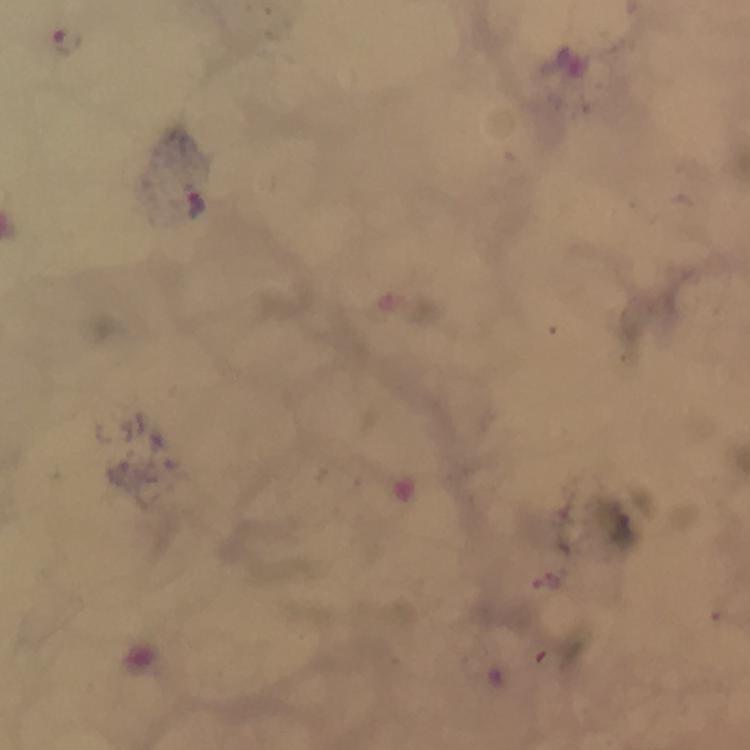
Approximate object centers, in pixels from the top-left corner.
Summary:
  - Plasmodium parasite locations: (x=66, y=43), (x=197, y=204)
  - Preparation: thick smear
  - Stain: Giemsa
  - Image size: 750×750 pixels
  - Capture: smartphone mounted on the microscope
  - Magnification: 100x
  - Immersion oil: applied
  - Cropped from: one field of view
  - Context: from a diagnostic examination for malaria